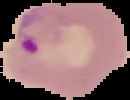
{
  "preparation": "thin blood film",
  "image_size": "130×100 pixels",
  "image_type": "segmented cell region with the area outside set to black",
  "malaria_status": "parasitized"
}